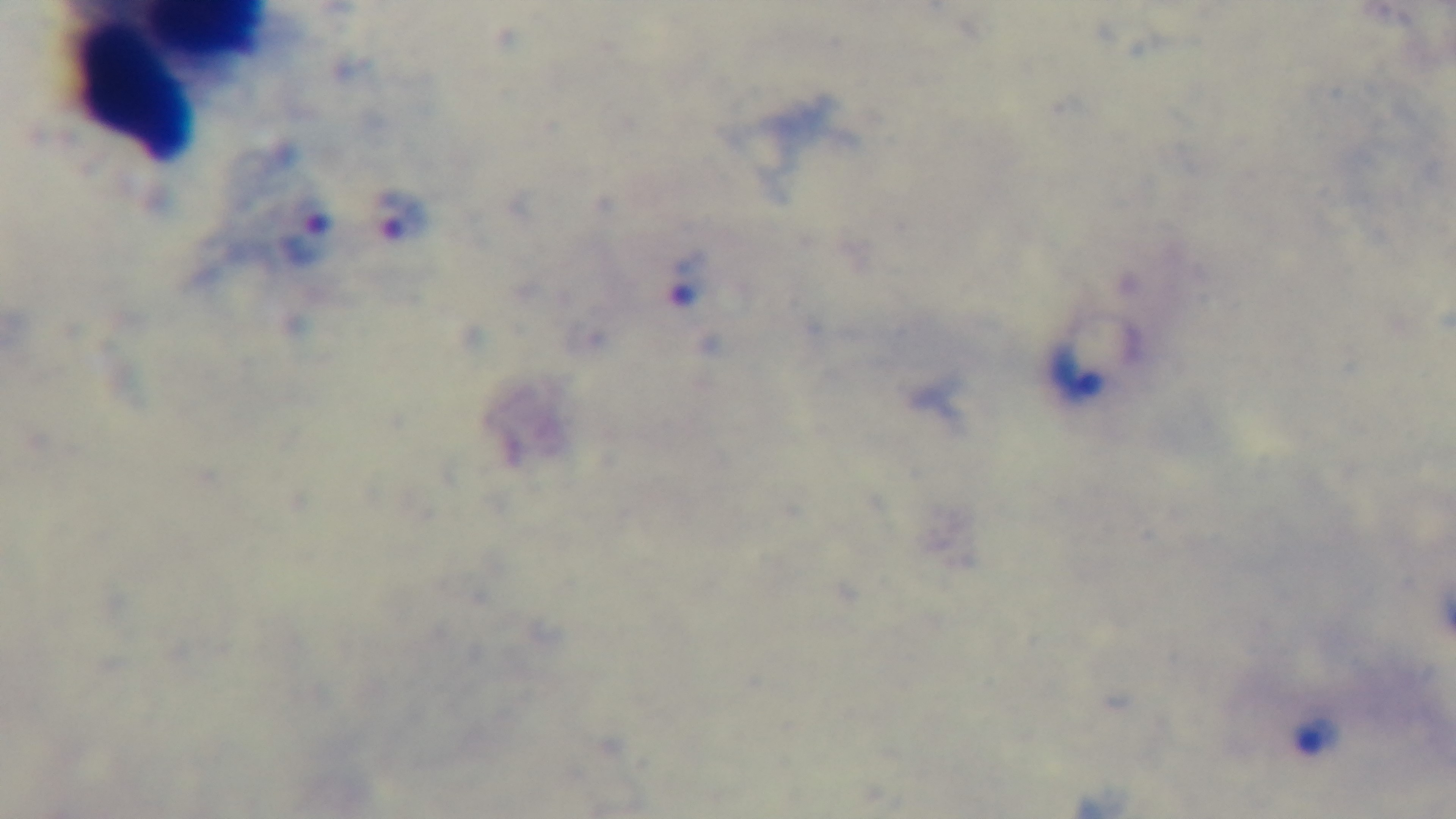

{
  "modality": "light microscopy",
  "objective": "100x oil immersion",
  "preparation": "thick blood film",
  "stain": "Giemsa",
  "field_of_view": "single",
  "capture": "mounted 4K digital camera",
  "malaria_status": "infected"
}